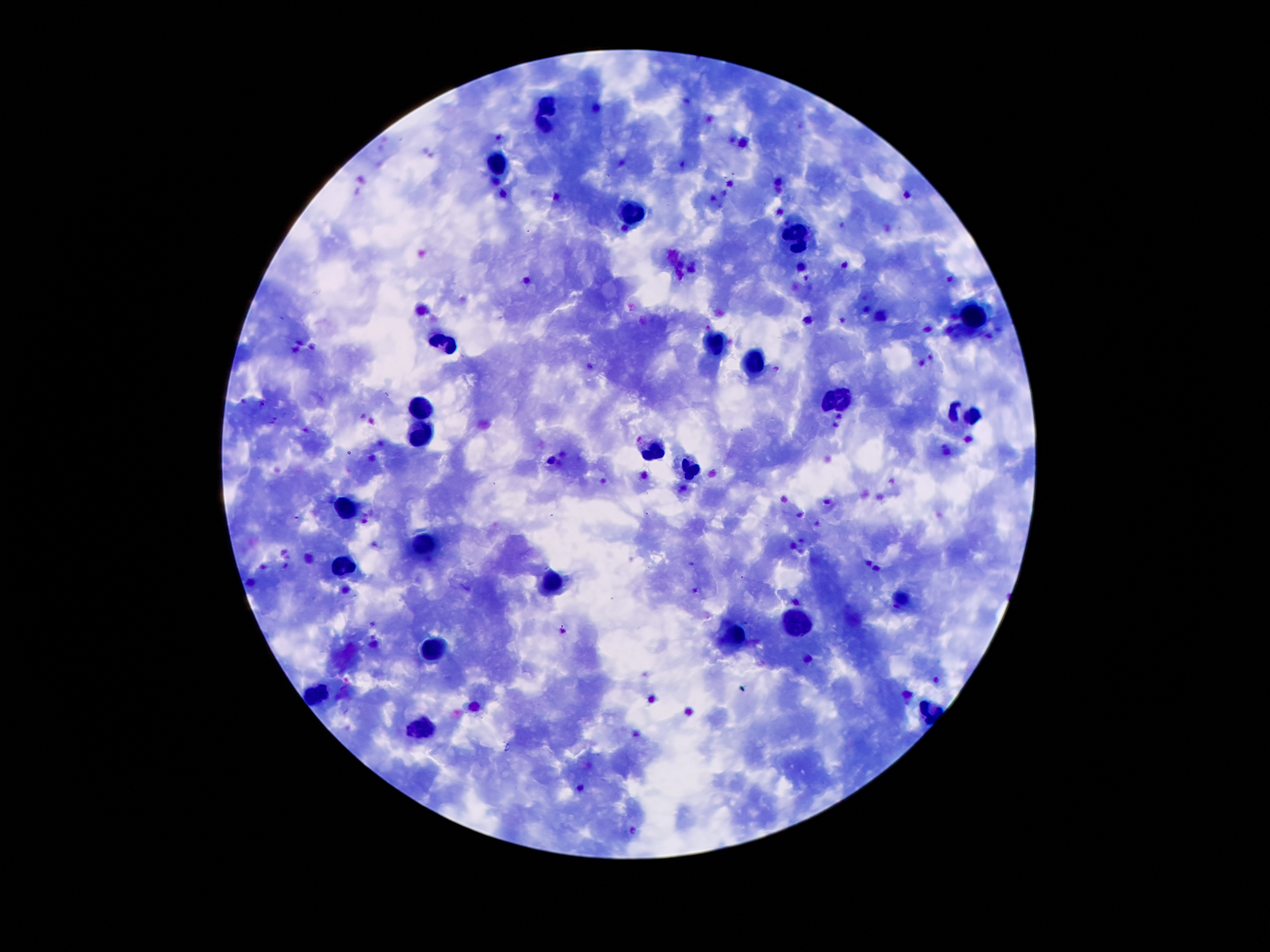 Giemsa stain. Thick blood film. Single field of view. 100x magnification. Photographed through the microscope eyepiece with a smartphone camera. Image is 1270×952 pixels. Patient malaria status: infected with Plasmodium falciparum.